Look for parasitized red blood cells.
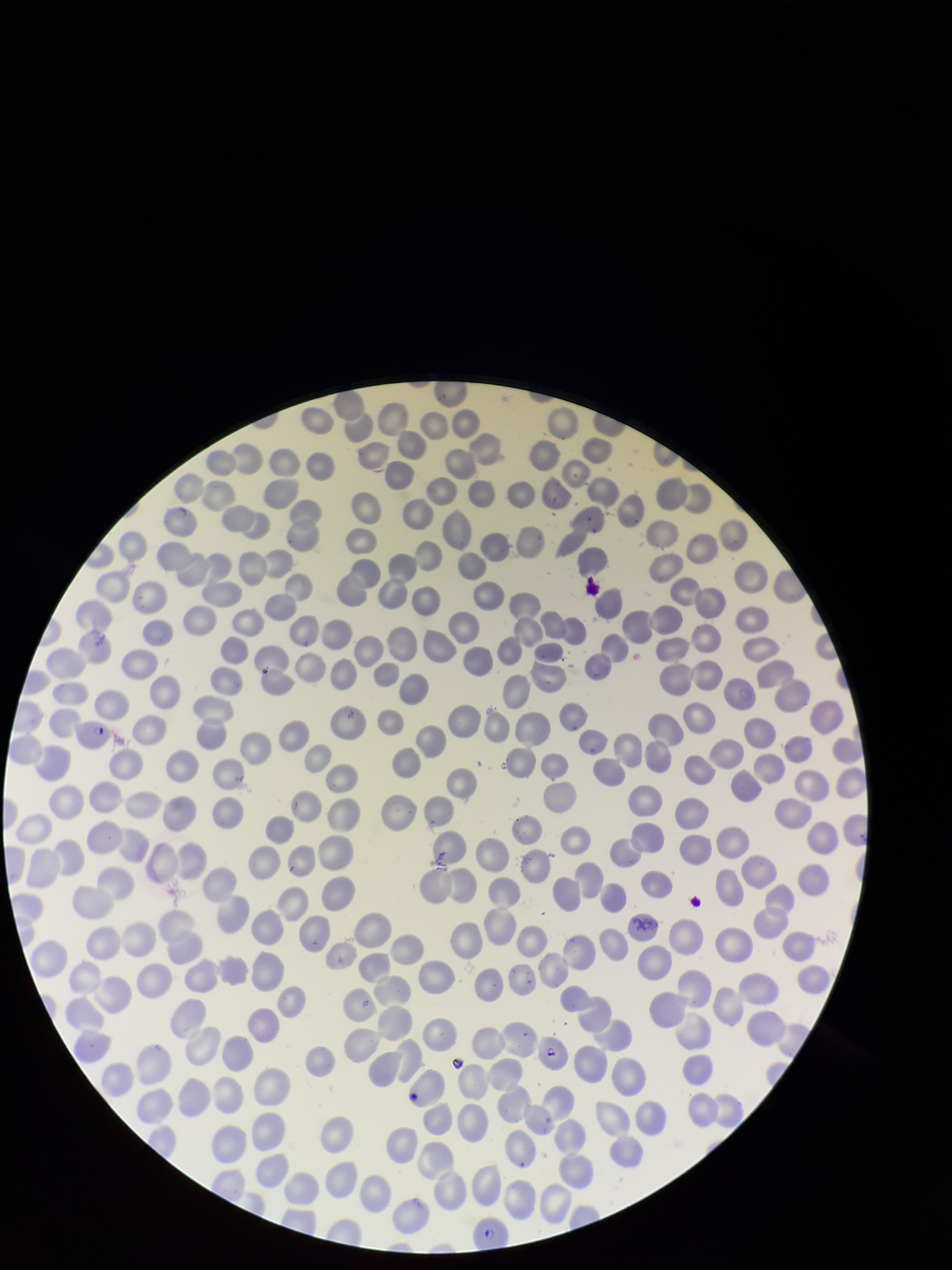
Seen.

One field from this slide. Patient malaria status: positive. Preparation: thin blood smear. Smartphone photograph taken through the eyepiece of a microscope. Parasitized red blood cell count: 3. Image is 952×1270 pixels. Stained with Giemsa. Species reported for this patient: Plasmodium falciparum. Red blood cell count: 276.